Report the malaria status of this cell.
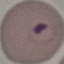
It is parasitized.

{
  "preparation": "thin blood film",
  "stain": "Giemsa",
  "image_type": "cell patch, automatically extracted from a larger field of view and resized to 64 × 64 pixels",
  "capture": "smartphone through the microscope eyepiece"
}